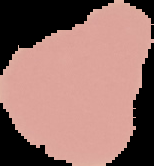

Summary:
  - Image size: 154×166 pixels
  - Preparation: thin blood film
  - Result: no Plasmodium parasites seen
  - Image type: segmented cell region with the area outside set to black